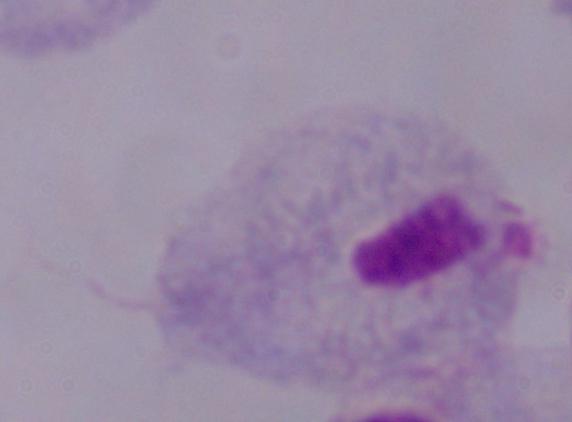

Summary:
  - Modality: micrograph
  - Magnification: 1000x
  - Identification: trichomonad